Locate every uninfected red blood cell.
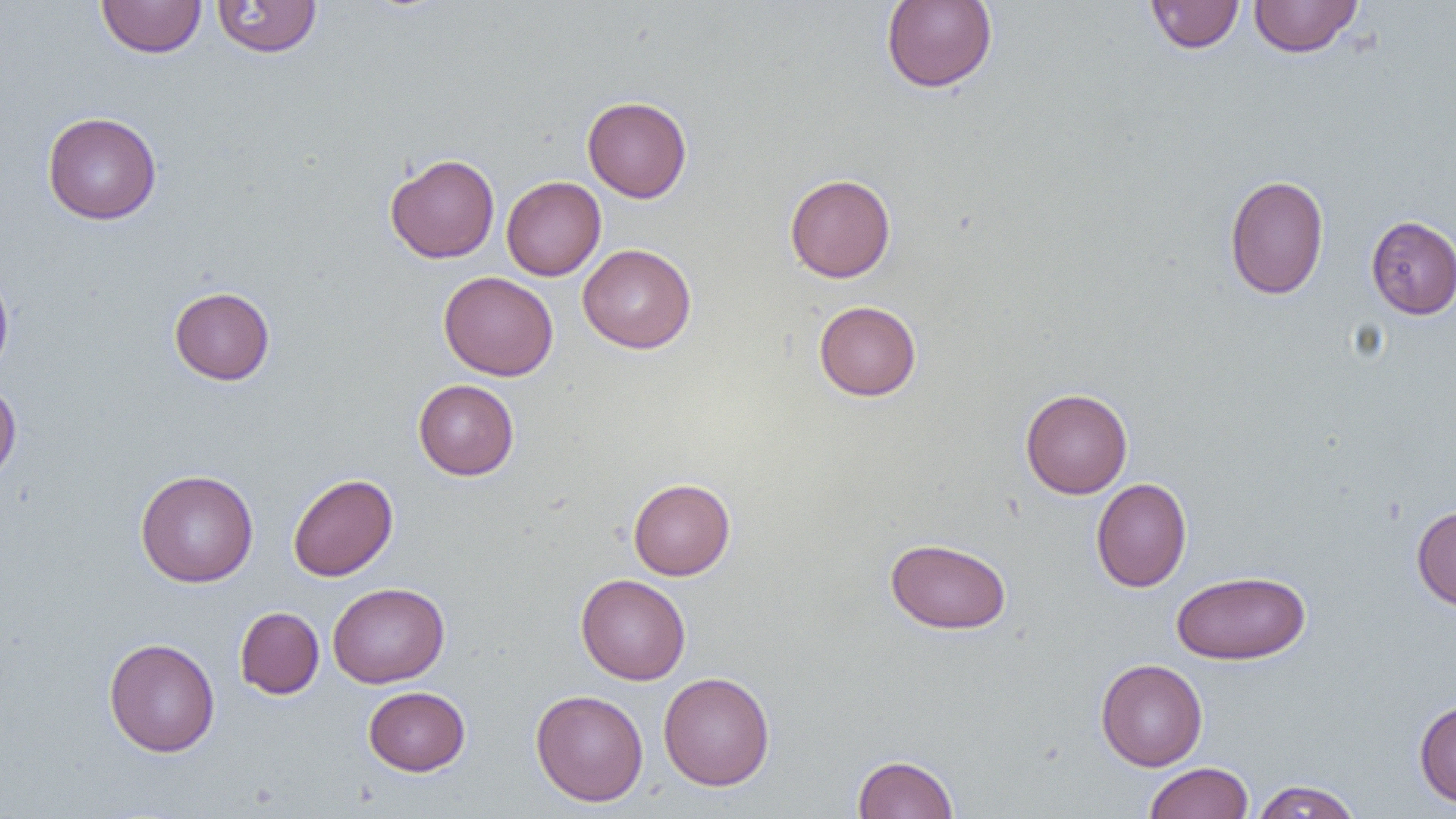

Approximate bounding boxes as (x1,y1)-(x2,y2) corner pairs in pixels.
Uninfected red blood cells: (96,0)-(206,58), (211,0)-(322,58), (881,0)-(997,92), (1145,0)-(1244,54), (1249,0)-(1363,58), (582,95)-(692,202), (42,111)-(162,225), (385,153)-(500,263), (784,173)-(896,282), (1224,175)-(1329,299), (502,176)-(606,280), (1366,215)-(1456,319), (578,243)-(696,353), (0,266)-(14,380), (438,271)-(558,381), (169,286)-(275,385), (814,300)-(921,401), (413,379)-(519,480), (0,380)-(21,483), (1020,388)-(1133,498), (135,469)-(258,587), (288,473)-(398,581), (628,478)-(736,580), (1091,478)-(1192,592), (1411,505)-(1456,611), (885,537)-(1011,634), (1171,570)-(1311,665), (576,574)-(691,685), (327,582)-(449,688), (235,607)-(324,699), (103,637)-(220,757), (1095,658)-(1208,771), (659,671)-(775,791), (363,686)-(470,776), (530,689)-(649,806), (1414,699)-(1456,807), (853,754)-(958,818), (1143,762)-(1254,819), (1251,780)-(1362,818).

Summary:
  - Slide-level diagnosis: negative for blood parasites
  - Image size: 1456×819 pixels
  - Field of view: one of a larger specimen
  - Preparation: thin blood film
  - Modality: optical microscopy
  - Magnification: 1000x